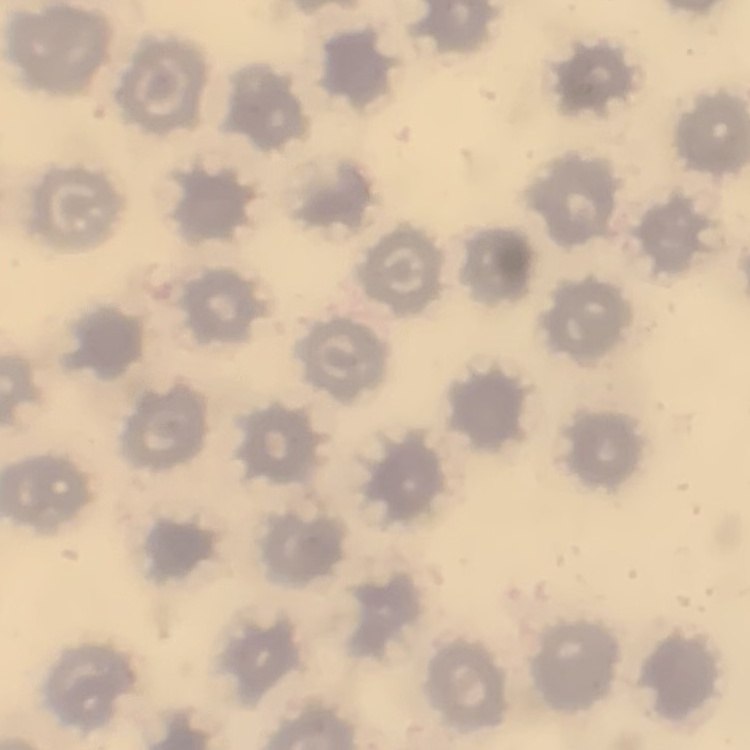
Summary:
  - Red blood cell morphology: no rouleaux formation
  - Image type: one tile cut from a larger photomicrograph
  - Stain: Field's or Giemsa
  - Preparation: thin blood film